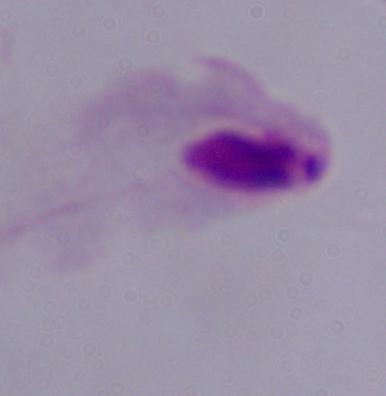
Summary:
  - Modality: photomicrograph
  - Identification: trichomonad
  - Magnification: 1000x